Report the malaria status of this cell.
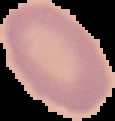
Uninfected.

{
  "preparation": "thin blood film",
  "image_size": "115×121 pixels",
  "image_type": "cell region segmented out of the field of view; surrounding area masked to black"
}